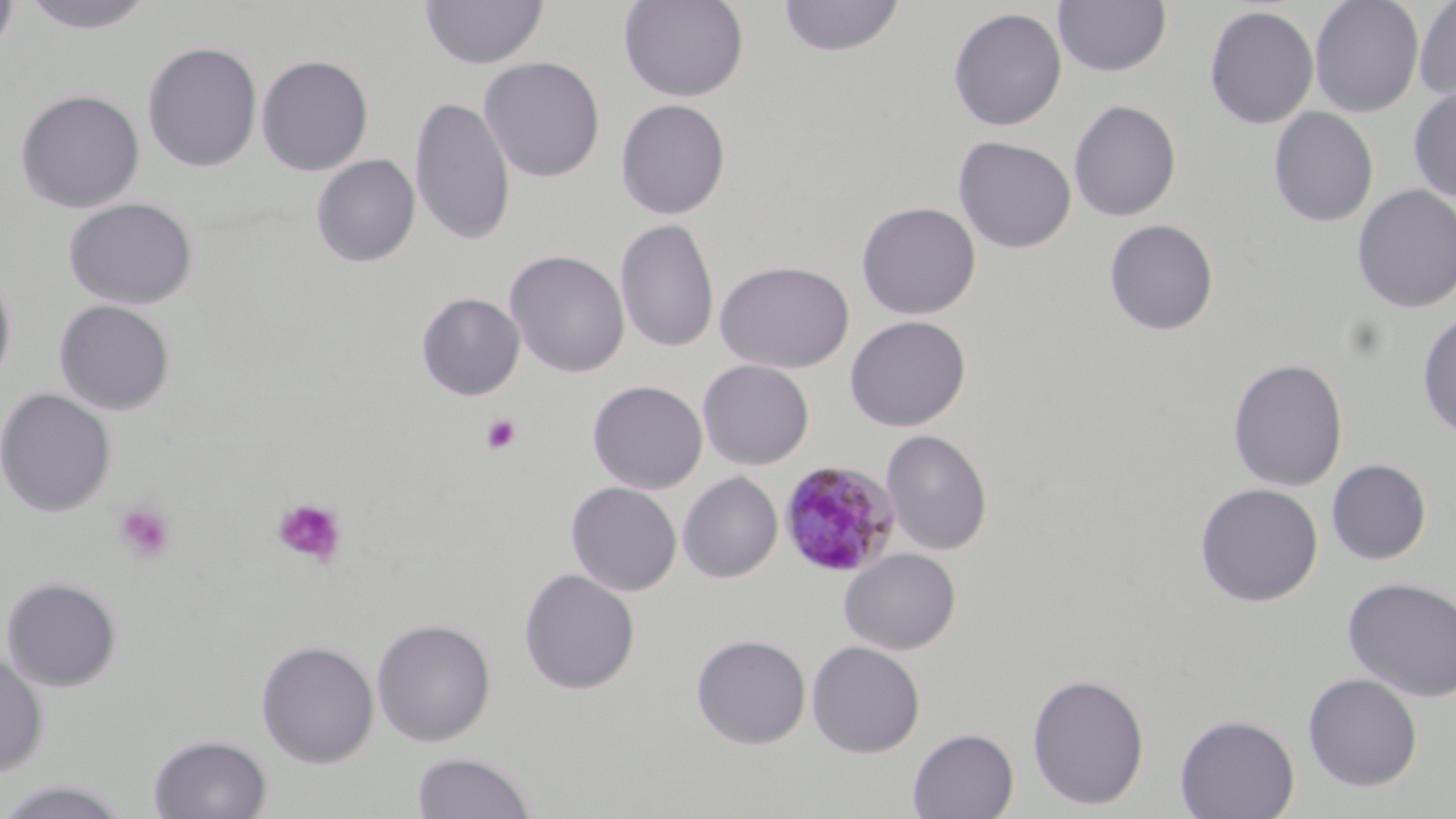
slide-level diagnosis = Plasmodium malariae
stain = May-Grünwald-Giemsa
field of view = one of a larger specimen
modality = light microscopy
platelet locations = approximate bounding boxes as (x1,y1)-(x2,y2) corner pairs in pixels: (480,413)-(522,456), (271,497)-(348,569), (113,501)-(177,565)
uninfected red blood cell locations = approximate bounding boxes as (x1,y1)-(x2,y2) corner pairs in pixels: (0,0)-(18,55), (19,0)-(156,34), (419,0)-(549,69), (618,0)-(750,102), (776,0)-(905,57), (1309,0)-(1424,118), (1415,0)-(1456,105), (1053,1)-(1171,77), (1204,6)-(1319,129), (948,7)-(1067,131), (141,41)-(263,172), (255,55)-(374,176), (478,56)-(605,182), (1408,84)-(1456,202), (15,89)-(145,213), (410,96)-(515,248), (615,99)-(730,219), (1068,99)-(1181,221), (1268,106)-(1378,227), (953,135)-(1076,253), (311,154)-(420,267), (1352,184)-(1456,313), (62,197)-(198,309), (856,201)-(981,320), (615,218)-(720,353), (1104,219)-(1219,336), (504,250)-(630,377), (714,260)-(854,373), (0,266)-(16,391), (416,292)-(525,400), (53,299)-(176,415), (1417,308)-(1456,438), (845,315)-(971,431), (1228,357)-(1348,492), (697,359)-(814,469), (587,379)-(708,494), (0,388)-(117,517), (880,429)-(993,556), (1326,458)-(1431,565), (678,472)-(783,582), (566,481)-(682,596), (1194,482)-(1323,607), (838,547)-(961,654), (519,568)-(640,695), (1,576)-(122,691), (1342,577)-(1456,703), (371,618)-(496,746), (691,633)-(811,749), (256,639)-(379,767), (806,640)-(925,758), (0,651)-(49,777), (1027,672)-(1149,810), (1302,672)-(1422,791), (1174,713)-(1300,819), (908,727)-(1019,819), (148,733)-(272,818), (412,750)-(535,818), (0,778)-(134,817)
Plasmodium malariae-infected red blood cell locations = approximate bounding boxes as (x1,y1)-(x2,y2) corner pairs in pixels: (777,459)-(901,579)
preparation = thin blood film
image size = 1456×819 pixels
magnification = 1000x